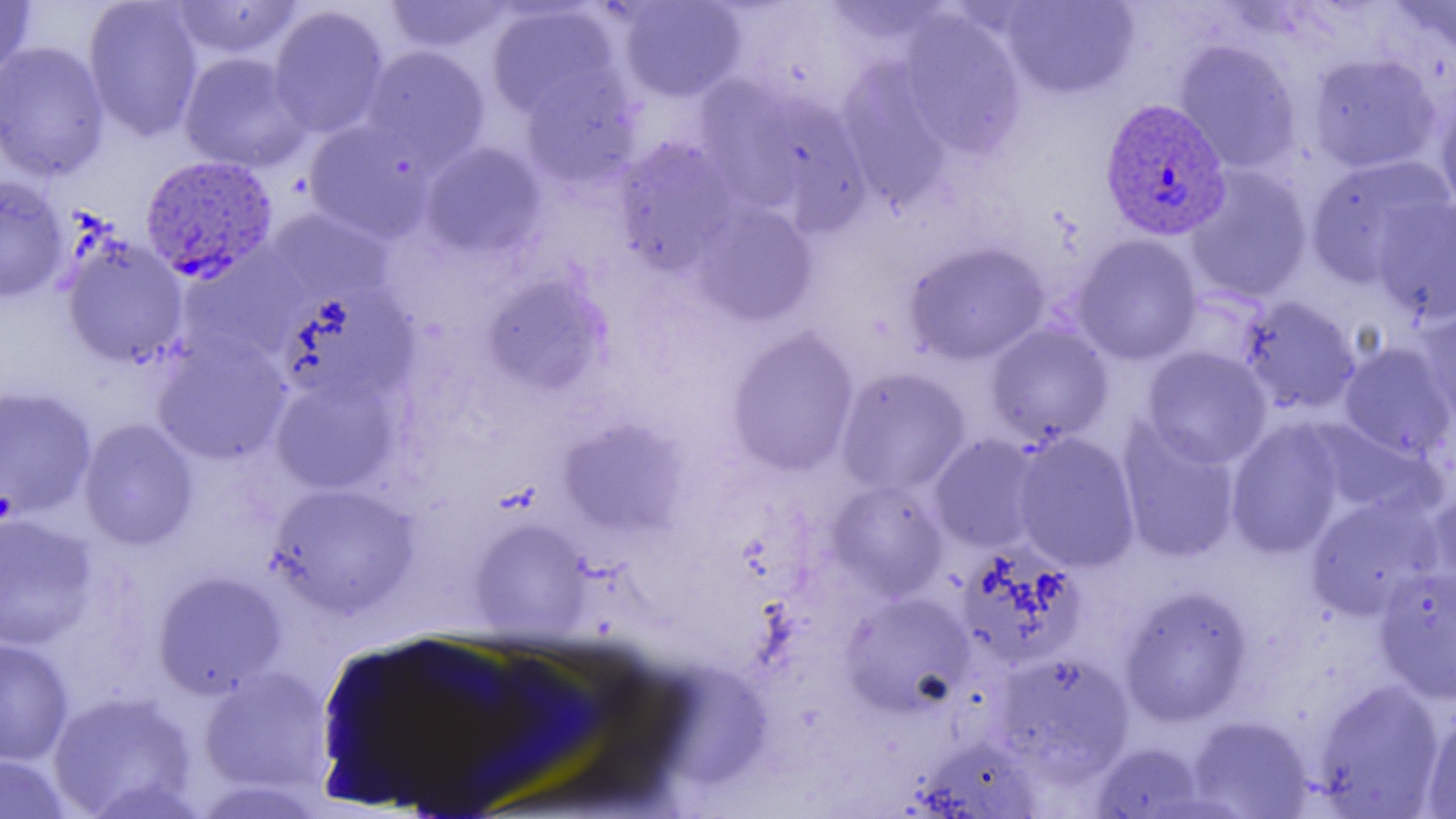
slide-level diagnosis = Plasmodium vivax
modality = light microscopy
field of view = one of a larger specimen
image size = 1456×819 pixels
uninfected red blood cell locations = approximate bounding boxes as (x1,y1)-(x2,y2) corner pairs in pixels: (0,0)-(37,81), (83,0)-(204,142), (383,0)-(514,54), (617,0)-(748,103), (1001,0)-(1139,99), (1389,0)-(1456,61), (167,1)-(305,60), (818,1)-(955,49), (485,3)-(620,119), (268,5)-(390,139), (897,9)-(1028,157), (1174,39)-(1302,173), (0,41)-(110,182), (361,45)-(491,169), (178,51)-(311,174), (1306,52)-(1442,174), (836,59)-(956,208), (519,68)-(642,189), (694,74)-(798,196), (1434,90)-(1456,217), (741,91)-(873,230), (302,119)-(435,243), (611,136)-(742,274), (420,142)-(548,260), (1304,154)-(1455,287), (1183,165)-(1314,303), (0,175)-(69,302), (1370,197)-(1456,324), (690,201)-(819,327), (265,208)-(392,304), (1071,234)-(1203,365), (59,235)-(189,367), (903,240)-(1051,365), (176,249)-(306,365), (481,273)-(611,394), (276,286)-(418,405), (1237,295)-(1361,415), (1415,304)-(1456,424), (985,323)-(1114,445), (726,327)-(860,476), (151,333)-(292,466), (1338,341)-(1456,460), (1140,346)-(1272,468), (835,367)-(972,496), (269,373)-(402,495), (0,386)-(97,518), (557,417)-(690,536), (78,418)-(199,550), (1116,419)-(1242,563), (1225,419)-(1345,558), (1307,422)-(1438,519), (1012,432)-(1140,573), (928,434)-(1045,554), (826,479)-(949,600), (266,483)-(419,617), (1420,485)-(1456,606), (1305,494)-(1445,620), (0,512)-(98,650), (470,518)-(591,639), (955,543)-(1087,669), (1373,566)-(1456,703), (151,570)-(287,698), (1119,585)-(1254,726), (840,590)-(975,716), (0,635)-(75,766), (990,651)-(1135,783), (198,666)-(333,794), (1312,679)-(1447,817), (46,690)-(199,818), (1421,709)-(1456,818), (1186,715)-(1314,818), (910,735)-(1045,817), (1089,741)-(1207,818), (0,753)-(73,819)
Plasmodium vivax-infected red blood cell locations = approximate bounding boxes as (x1,y1)-(x2,y2) corner pairs in pixels: (1100,93)-(1233,238), (140,153)-(279,283)
magnification = 1000x
preparation = thin blood film